Point out each malaria parasite.
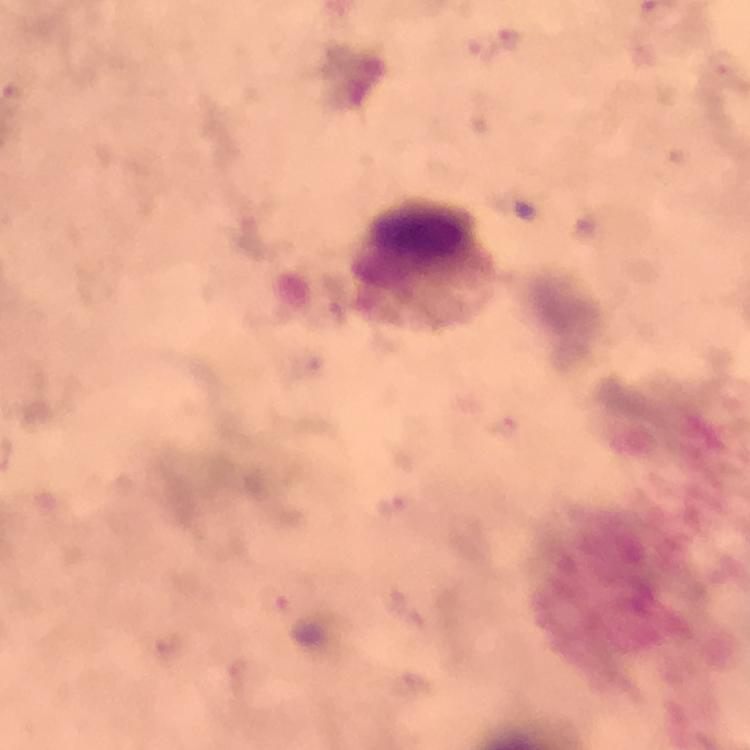
Approximate centers as (x, y) in pixels.
Malaria parasites: (394, 506), (277, 604).

Summary:
  - Leukocyte locations: (424, 266)
  - Cropped from: one field of view
  - Stain: Giemsa
  - Context: from a diagnostic examination for malaria
  - Immersion oil: applied
  - Image size: 750×750 pixels
  - Magnification: 100x
  - Capture: smartphone mounted on the microscope
  - Preparation: thick smear